State which parasite is depicted.
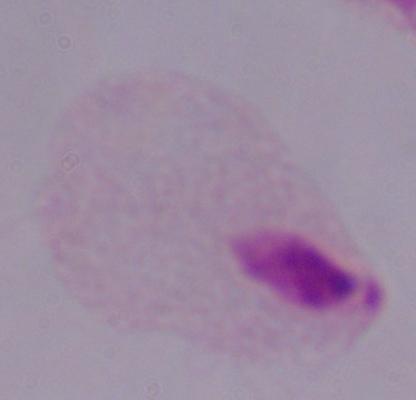
A trichomonad.

modality = micrograph
magnification = 1000x